Describe the morphology of the red blood cells.
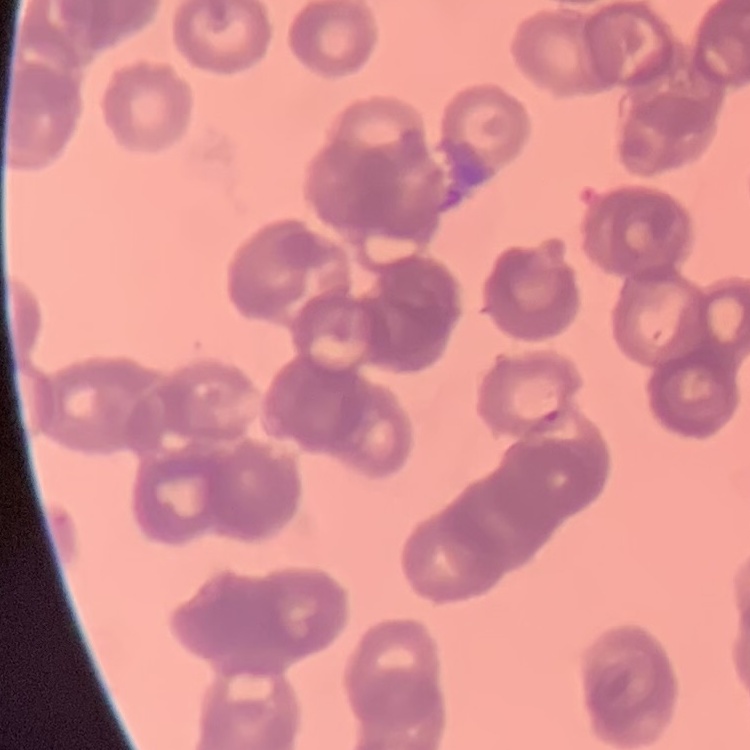

They show rouleaux formation.

Summary:
  - Image type: one tile cut from a larger photomicrograph
  - Preparation: thin peripheral smear
  - Stain: Field's or Giemsa